Describe the morphology of the red blood cells.
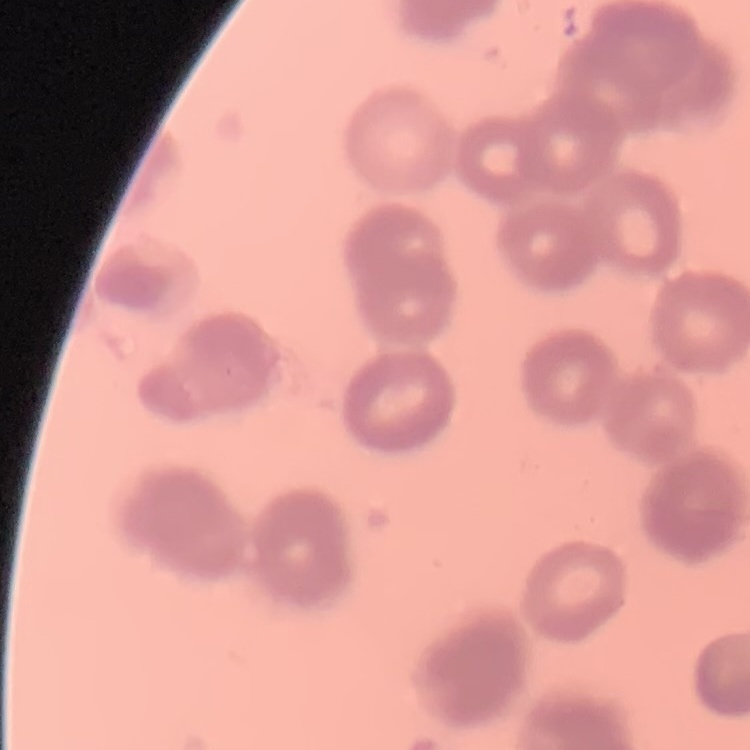

They show rouleaux formation.

stain = Field's or Giemsa
preparation = thin blood smear
image type = one tile cut from a larger photomicrograph